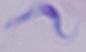

{
  "modality": "micrograph",
  "magnification": "1000x",
  "identification": "trypanosome"
}